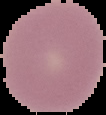

Image is 106×115 pixels. From a thin blood film. Segmented cell region on a black background. Malaria status: uninfected.